Identify the parasite.
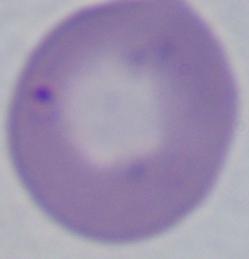

Babesia.

modality = photomicrograph
magnification = 1000x